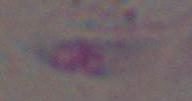
Photomicrograph. Toxoplasma gondii is seen. Captured at 1000x magnification.